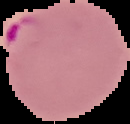
Summary:
  - Image type: segmented cell region with the area outside set to black
  - Image size: 130×124 pixels
  - Preparation: thin blood smear
  - Result: malaria parasites identified